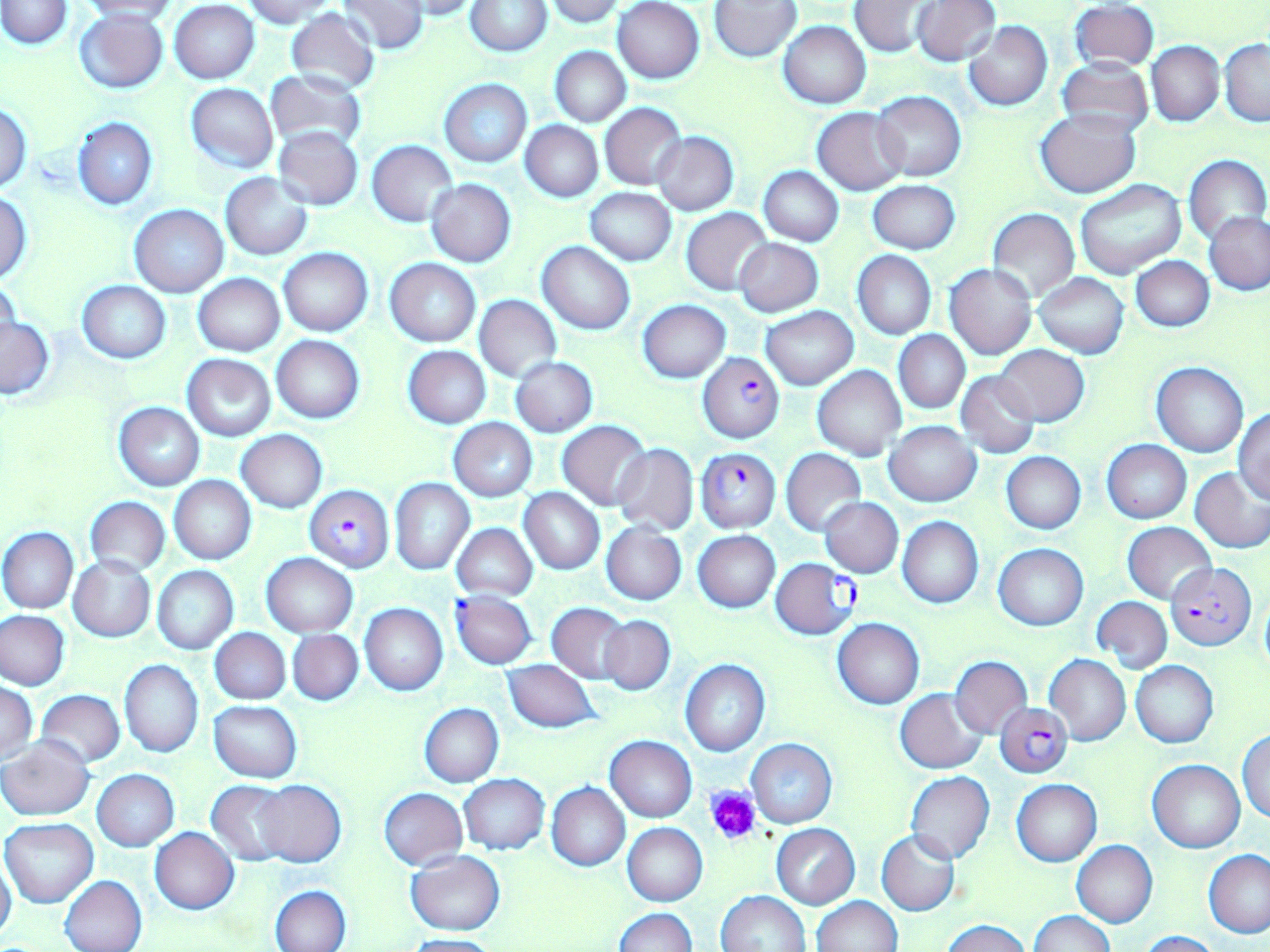

Approximate bounding boxes as (x1,y1)-(x2,y2) corner pairs in pixels. Plasmodium falciparum-infected red blood cell locations: (698,354)-(785,443), (695,446)-(781,531), (306,484)-(393,572), (770,558)-(860,639), (1166,563)-(1254,651), (452,592)-(536,668), (995,703)-(1072,779). Platelet locations: (705,787)-(760,845). Uninfected red blood cell locations: (1,0)-(71,48), (337,0)-(429,54), (391,0)-(482,20), (542,0)-(625,25), (913,0)-(999,65), (79,1)-(180,22), (243,1)-(340,24), (613,1)-(705,83), (849,1)-(934,57), (170,2)-(260,83), (466,2)-(552,56), (710,2)-(801,61), (1071,3)-(1158,70), (284,8)-(380,95), (74,9)-(169,93), (963,20)-(1053,111), (779,21)-(871,108), (1219,40)-(1270,126), (1147,42)-(1224,126), (551,46)-(630,126), (1056,60)-(1154,136), (265,69)-(368,152), (439,79)-(532,167), (186,83)-(278,173), (872,91)-(966,182), (0,102)-(32,192), (600,103)-(687,189), (813,107)-(908,195), (1037,110)-(1143,198), (72,117)-(157,210), (520,121)-(603,202), (274,127)-(363,210), (652,132)-(739,216), (368,140)-(458,227), (1184,154)-(1269,246), (757,166)-(843,246), (220,174)-(312,259), (426,180)-(516,266), (868,180)-(960,254), (1075,180)-(1187,280), (585,188)-(676,265), (0,192)-(32,283), (130,205)-(228,296), (681,208)-(771,295), (988,209)-(1079,300), (1205,211)-(1270,295), (734,238)-(824,318), (538,241)-(635,335), (278,246)-(373,336), (852,251)-(936,339), (1131,256)-(1214,332), (384,258)-(480,347), (946,264)-(1036,359), (1033,272)-(1129,358), (194,273)-(285,356), (0,281)-(21,357), (78,281)-(170,363), (475,294)-(561,382), (638,300)-(730,383), (760,307)-(859,390), (1,315)-(54,399), (894,331)-(969,413), (273,335)-(365,422), (404,345)-(491,428), (994,346)-(1089,427), (182,355)-(275,442), (510,356)-(598,437), (1152,361)-(1248,457), (813,365)-(907,461), (955,370)-(1040,457), (114,402)-(205,491), (1233,408)-(1270,503), (449,418)-(537,501), (557,420)-(651,510), (884,421)-(981,506), (236,430)-(327,512), (1103,439)-(1190,524), (612,442)-(698,536), (782,449)-(865,535), (1002,453)-(1085,534), (1190,467)-(1270,554), (168,476)-(256,565), (390,478)-(474,574), (518,487)-(605,575), (85,497)-(169,575), (820,497)-(903,577), (898,517)-(984,607), (601,521)-(687,604), (1123,522)-(1216,606), (453,524)-(537,601), (1,527)-(77,613), (693,530)-(780,612), (994,544)-(1089,630), (262,553)-(358,637), (69,555)-(157,643), (152,565)-(237,654), (1093,597)-(1172,671), (360,603)-(447,696), (547,603)-(632,684), (0,610)-(70,690), (599,615)-(675,695), (833,618)-(924,709), (210,629)-(289,704), (288,629)-(362,705), (1044,655)-(1131,746), (949,656)-(1031,736), (503,659)-(599,732), (120,660)-(203,757), (681,660)-(770,757), (1130,660)-(1218,747), (1,683)-(38,763), (895,688)-(988,774), (35,690)-(125,767), (209,701)-(302,782), (420,703)-(504,787), (1237,728)-(1269,822), (605,735)-(697,821), (2,737)-(94,821), (746,739)-(838,828), (1148,759)-(1245,853), (92,770)-(179,852), (906,772)-(995,864), (458,775)-(549,855), (1012,779)-(1101,866), (253,780)-(345,867), (206,781)-(293,866), (547,783)-(630,871), (380,788)-(467,870), (2,819)-(99,907), (622,823)-(707,906), (771,824)-(859,909), (150,828)-(238,914), (877,829)-(960,916), (1072,841)-(1157,927), (1204,850)-(1270,938), (404,851)-(505,935), (0,853)-(16,946), (60,875)-(147,952), (271,886)-(351,951), (717,890)-(811,951), (811,896)-(902,952), (614,908)-(698,952), (1030,912)-(1116,952), (943,920)-(1029,952), (1136,930)-(1221,952), (402,934)-(501,952). Slide-level diagnosis: Plasmodium falciparum. Single field of view. Thin blood smear. Captured at 1000x magnification. Light microscopy. May-Grünwald-Giemsa-stained preparation. Image is 1270×952 pixels.